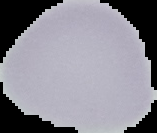

image_type: cell region segmented out of the field of view; surrounding area masked to black
preparation: thin blood film
image_size: 157×133 pixels
malaria_status: uninfected